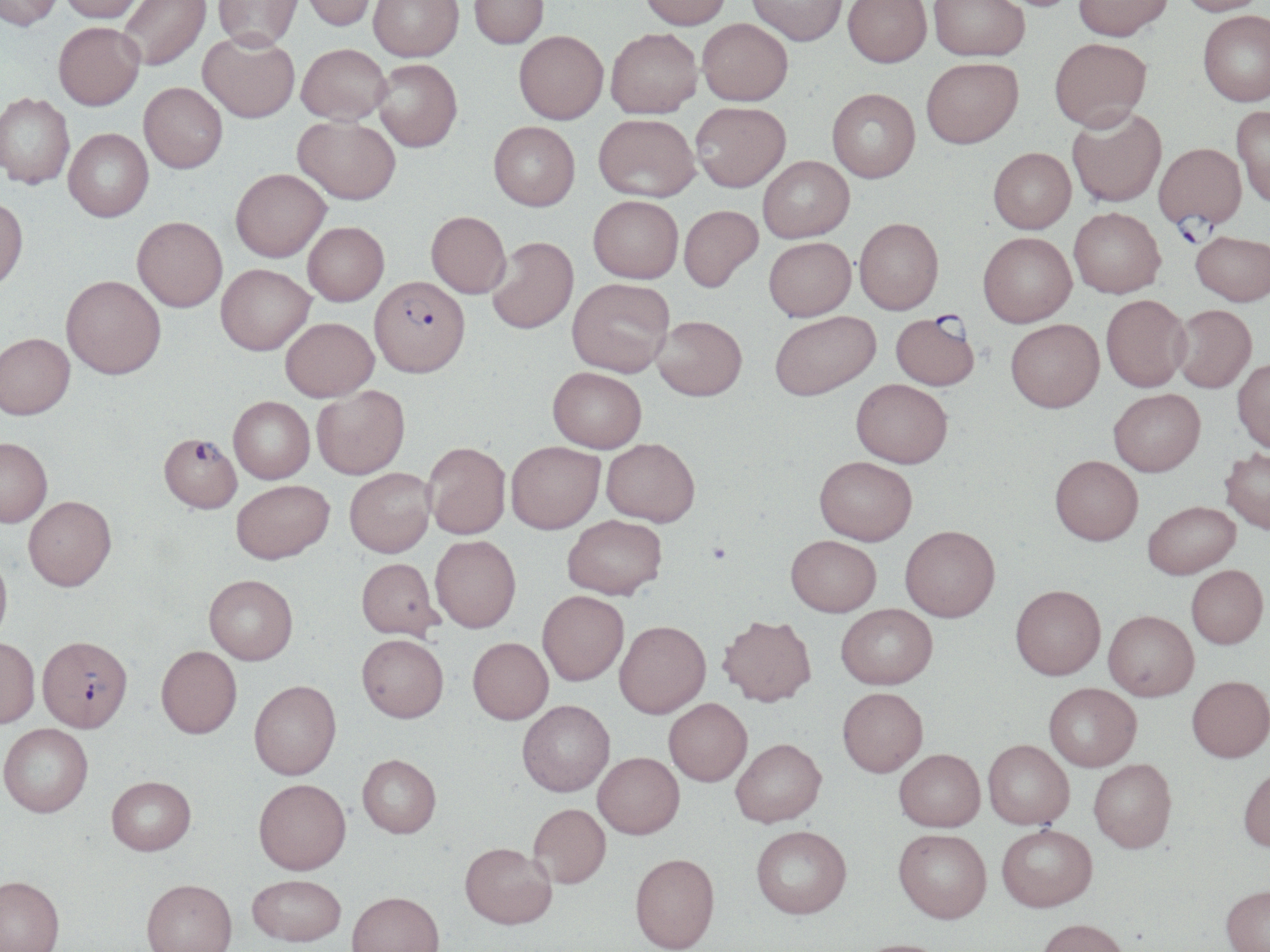

Plasmodium falciparum-infected red blood cell locations = approximate bounding boxes as named x1/y1/x2/y2 corners in pixels: (x1=1154, y1=143, x2=1247, y2=248), (x1=370, y1=275, x2=470, y2=377), (x1=890, y1=314, x2=979, y2=392), (x1=159, y1=432, x2=242, y2=513), (x1=37, y1=640, x2=133, y2=737)
slide-level diagnosis = Plasmodium falciparum
image size = 1270×952 pixels
uninfected red blood cell locations = approximate bounding boxes as named x1/y1/x2/y2 corners in pixels: (x1=0, y1=0, x2=63, y2=30), (x1=61, y1=0, x2=147, y2=23), (x1=119, y1=0, x2=211, y2=70), (x1=213, y1=0, x2=303, y2=51), (x1=300, y1=0, x2=378, y2=31), (x1=369, y1=0, x2=463, y2=61), (x1=469, y1=0, x2=549, y2=48), (x1=640, y1=0, x2=731, y2=30), (x1=747, y1=0, x2=848, y2=46), (x1=843, y1=0, x2=932, y2=68), (x1=928, y1=0, x2=1028, y2=62), (x1=1073, y1=0, x2=1173, y2=42), (x1=1176, y1=0, x2=1266, y2=17), (x1=1198, y1=10, x2=1269, y2=106), (x1=698, y1=18, x2=793, y2=106), (x1=53, y1=22, x2=145, y2=110), (x1=606, y1=28, x2=702, y2=118), (x1=514, y1=30, x2=608, y2=123), (x1=198, y1=31, x2=300, y2=122), (x1=1050, y1=39, x2=1151, y2=133), (x1=297, y1=43, x2=391, y2=125), (x1=373, y1=59, x2=462, y2=151), (x1=922, y1=59, x2=1023, y2=151), (x1=139, y1=82, x2=227, y2=173), (x1=827, y1=89, x2=920, y2=184), (x1=0, y1=93, x2=75, y2=189), (x1=691, y1=101, x2=790, y2=192), (x1=1232, y1=105, x2=1270, y2=208), (x1=1066, y1=108, x2=1167, y2=208), (x1=594, y1=114, x2=700, y2=202), (x1=292, y1=115, x2=401, y2=204), (x1=489, y1=121, x2=580, y2=211), (x1=63, y1=129, x2=153, y2=221), (x1=988, y1=149, x2=1076, y2=235), (x1=758, y1=156, x2=854, y2=243), (x1=231, y1=168, x2=330, y2=261), (x1=588, y1=195, x2=683, y2=283), (x1=0, y1=197, x2=28, y2=291), (x1=679, y1=205, x2=763, y2=291), (x1=1069, y1=208, x2=1165, y2=300), (x1=426, y1=211, x2=510, y2=298), (x1=132, y1=216, x2=227, y2=311), (x1=854, y1=218, x2=943, y2=314), (x1=303, y1=222, x2=389, y2=306), (x1=1191, y1=232, x2=1270, y2=306), (x1=978, y1=233, x2=1077, y2=328), (x1=487, y1=236, x2=578, y2=334), (x1=763, y1=237, x2=856, y2=320), (x1=216, y1=263, x2=316, y2=354), (x1=61, y1=275, x2=166, y2=378), (x1=567, y1=278, x2=674, y2=377), (x1=1102, y1=295, x2=1191, y2=393), (x1=1171, y1=305, x2=1256, y2=393), (x1=770, y1=311, x2=880, y2=400), (x1=652, y1=315, x2=747, y2=400), (x1=281, y1=317, x2=378, y2=401), (x1=1005, y1=319, x2=1104, y2=413), (x1=0, y1=333, x2=75, y2=420), (x1=1233, y1=358, x2=1270, y2=453), (x1=547, y1=366, x2=646, y2=452), (x1=851, y1=379, x2=952, y2=467), (x1=311, y1=385, x2=410, y2=479), (x1=1109, y1=389, x2=1205, y2=476), (x1=228, y1=396, x2=315, y2=483), (x1=0, y1=437, x2=52, y2=528), (x1=601, y1=438, x2=700, y2=526), (x1=506, y1=440, x2=605, y2=533), (x1=423, y1=441, x2=511, y2=539), (x1=1220, y1=448, x2=1270, y2=534), (x1=1050, y1=455, x2=1143, y2=544), (x1=814, y1=456, x2=917, y2=545), (x1=345, y1=467, x2=436, y2=557), (x1=231, y1=479, x2=335, y2=564), (x1=23, y1=496, x2=117, y2=593), (x1=1143, y1=501, x2=1240, y2=578), (x1=563, y1=515, x2=667, y2=600), (x1=900, y1=525, x2=999, y2=621), (x1=430, y1=535, x2=521, y2=632), (x1=786, y1=535, x2=881, y2=616), (x1=0, y1=552, x2=12, y2=649), (x1=356, y1=558, x2=443, y2=642), (x1=1186, y1=565, x2=1268, y2=648), (x1=204, y1=576, x2=298, y2=666), (x1=1010, y1=584, x2=1106, y2=679), (x1=537, y1=591, x2=629, y2=686), (x1=836, y1=603, x2=937, y2=688), (x1=1104, y1=610, x2=1198, y2=700), (x1=718, y1=614, x2=816, y2=706), (x1=614, y1=620, x2=711, y2=718), (x1=356, y1=634, x2=448, y2=724), (x1=468, y1=638, x2=553, y2=725), (x1=0, y1=640, x2=40, y2=732), (x1=156, y1=648, x2=241, y2=741), (x1=1187, y1=675, x2=1270, y2=762), (x1=249, y1=682, x2=341, y2=780), (x1=1044, y1=682, x2=1141, y2=770), (x1=837, y1=687, x2=928, y2=776), (x1=664, y1=698, x2=752, y2=786), (x1=517, y1=700, x2=615, y2=797), (x1=0, y1=726, x2=93, y2=820), (x1=731, y1=738, x2=826, y2=826), (x1=983, y1=739, x2=1074, y2=829), (x1=894, y1=748, x2=985, y2=831), (x1=593, y1=752, x2=684, y2=838), (x1=357, y1=754, x2=441, y2=838), (x1=1088, y1=759, x2=1176, y2=852), (x1=1238, y1=765, x2=1270, y2=852), (x1=107, y1=777, x2=196, y2=857), (x1=254, y1=779, x2=351, y2=875), (x1=528, y1=803, x2=611, y2=888), (x1=997, y1=824, x2=1097, y2=911), (x1=751, y1=825, x2=851, y2=918), (x1=893, y1=828, x2=992, y2=923), (x1=461, y1=842, x2=556, y2=930), (x1=629, y1=853, x2=720, y2=951), (x1=247, y1=875, x2=346, y2=946), (x1=0, y1=878, x2=65, y2=952), (x1=141, y1=881, x2=237, y2=952), (x1=1220, y1=884, x2=1270, y2=952), (x1=347, y1=892, x2=444, y2=952), (x1=1036, y1=918, x2=1130, y2=952), (x1=852, y1=938, x2=953, y2=952)
modality = light microscopy
field of view = one of a larger specimen
preparation = thin blood film
stain = May-Grünwald-Giemsa
magnification = 1000x